Assess this cell for malaria.
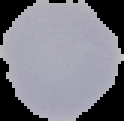

Uninfected.

preparation: thin blood film
image_type: cell region segmented out of the field of view; surrounding area masked to black
image_size: 124×121 pixels